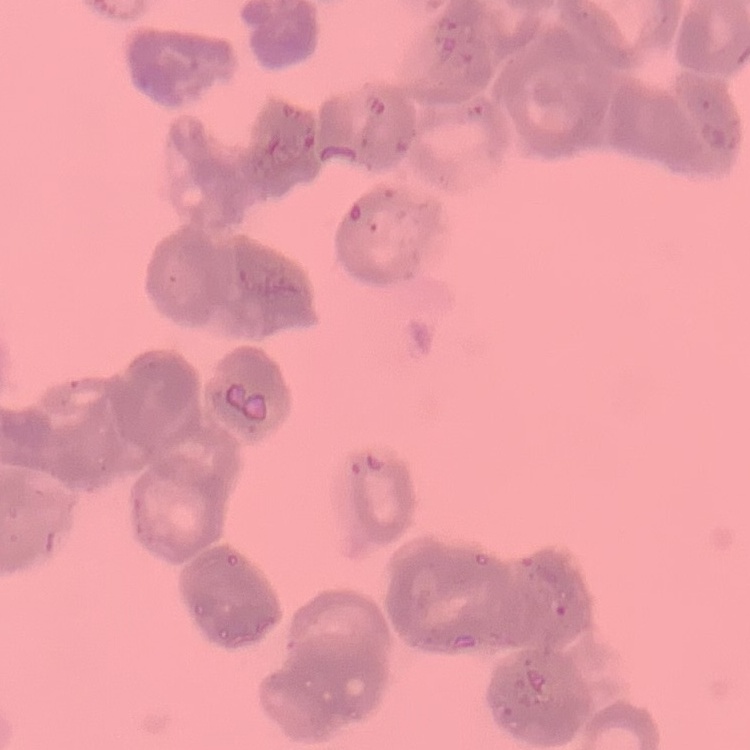
The erythrocytes exhibit rouleaux formation. Thin blood film. Field's or Giemsa stain. Square crop of a larger photomicrograph.